Locate and identify every blood parasite.
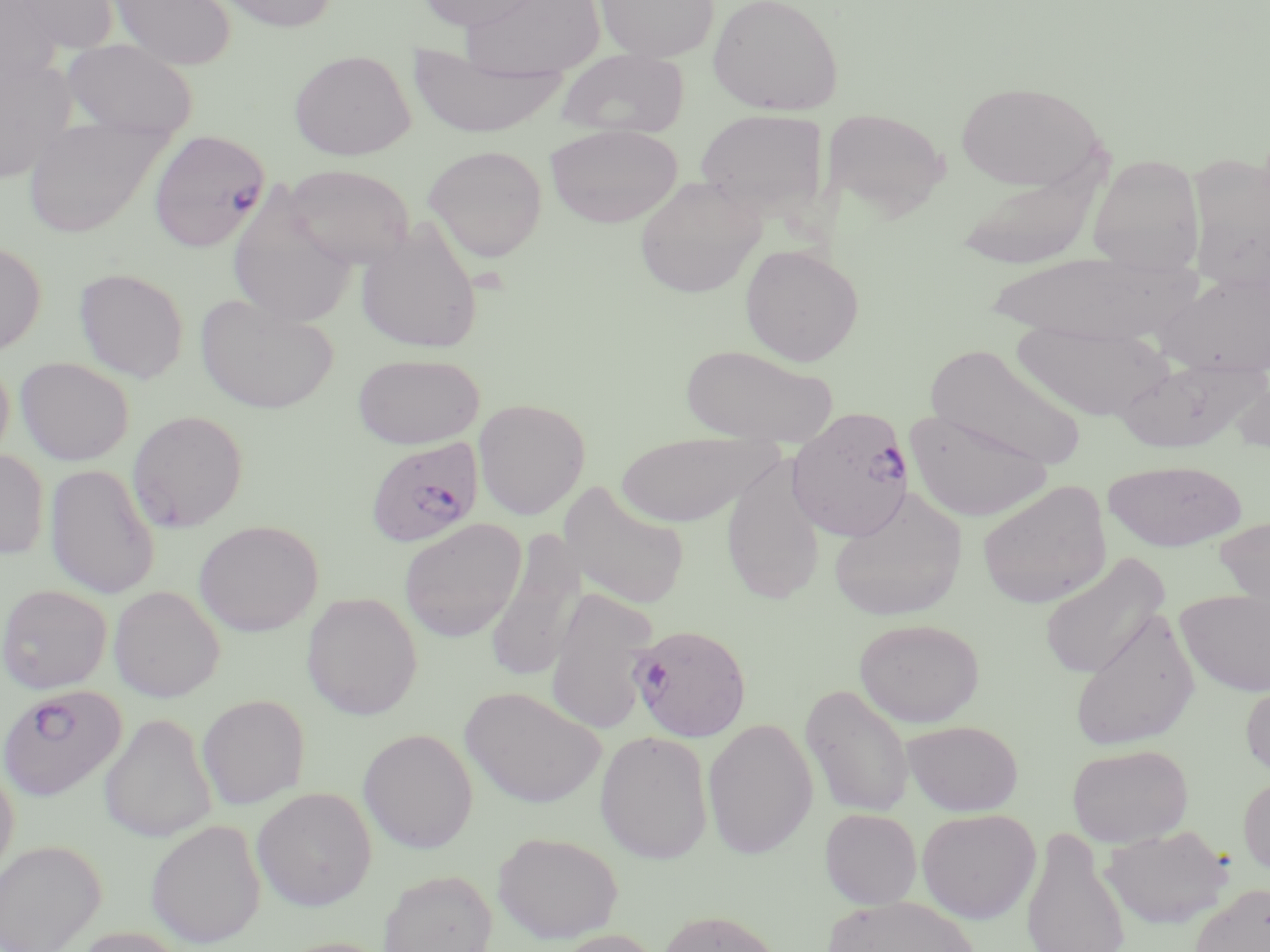

Approximate bounding boxes as (x1, y1, x2, y2) in pixels.
Plasmodium falciparum-infected red blood cells: (148, 129, 270, 252), (786, 406, 916, 542), (365, 435, 487, 548), (623, 623, 759, 743), (0, 685, 127, 801).
No Plasmodium ovale, Plasmodium malariae, Plasmodium vivax, Babesia divergens, or Trypanosoma brucei observed.

Uninfected red blood cell locations: (5, 0, 115, 62), (108, 0, 236, 70), (213, 0, 340, 33), (416, 0, 546, 31), (462, 0, 606, 79), (594, 0, 720, 63), (708, 0, 844, 116), (0, 1, 61, 87), (62, 39, 198, 138), (405, 45, 570, 139), (557, 48, 689, 139), (288, 49, 416, 161), (0, 53, 76, 184), (954, 81, 1107, 192), (695, 108, 829, 220), (824, 108, 949, 222), (22, 116, 169, 238), (545, 124, 683, 228), (424, 145, 548, 262), (1187, 152, 1270, 292), (1087, 153, 1205, 275), (955, 159, 1105, 270), (284, 164, 416, 268), (635, 176, 766, 298), (226, 185, 359, 330), (355, 221, 484, 354), (0, 240, 47, 355), (739, 243, 864, 366), (988, 250, 1198, 344), (74, 267, 189, 383), (1155, 269, 1270, 380), (194, 293, 338, 414), (1012, 320, 1173, 422), (679, 343, 839, 445), (924, 343, 1087, 470), (352, 353, 485, 449), (0, 356, 14, 466), (15, 357, 133, 465), (1115, 357, 1266, 453), (1231, 370, 1270, 454), (474, 398, 591, 520), (904, 408, 1054, 523), (127, 410, 248, 533), (613, 433, 775, 526), (0, 449, 49, 559), (720, 456, 827, 606), (1103, 458, 1246, 552), (45, 463, 160, 600), (977, 479, 1112, 609), (557, 481, 690, 610), (828, 490, 968, 622), (1213, 517, 1270, 623), (399, 518, 527, 642), (194, 520, 323, 636), (484, 532, 585, 685), (1038, 552, 1170, 681), (0, 584, 112, 694), (108, 585, 225, 702), (545, 586, 659, 735), (1176, 589, 1270, 697), (301, 591, 423, 720), (1070, 608, 1201, 752), (853, 618, 985, 727), (1240, 677, 1270, 781), (800, 683, 916, 819), (460, 686, 606, 808), (197, 694, 310, 809), (100, 713, 217, 843), (702, 717, 818, 859), (901, 720, 1024, 816), (358, 728, 478, 853), (594, 729, 714, 864), (1067, 743, 1193, 847), (0, 758, 19, 883), (1237, 773, 1270, 877), (252, 786, 377, 911), (916, 807, 1041, 924), (820, 808, 922, 909), (146, 819, 266, 948), (1101, 824, 1235, 929), (1021, 828, 1130, 952), (493, 831, 623, 943), (0, 839, 106, 951), (378, 869, 497, 952), (1188, 883, 1270, 952), (822, 896, 981, 952), (656, 909, 784, 952), (68, 925, 190, 952), (547, 928, 667, 952). Slide-level diagnosis: Plasmodium falciparum. One field of a larger specimen. Thin blood film. Optical microscopy. Captured at 1000x magnification. Image is 1270×952 pixels. May-Grünwald-Giemsa stain.